Outline each blood parasite and name the species.
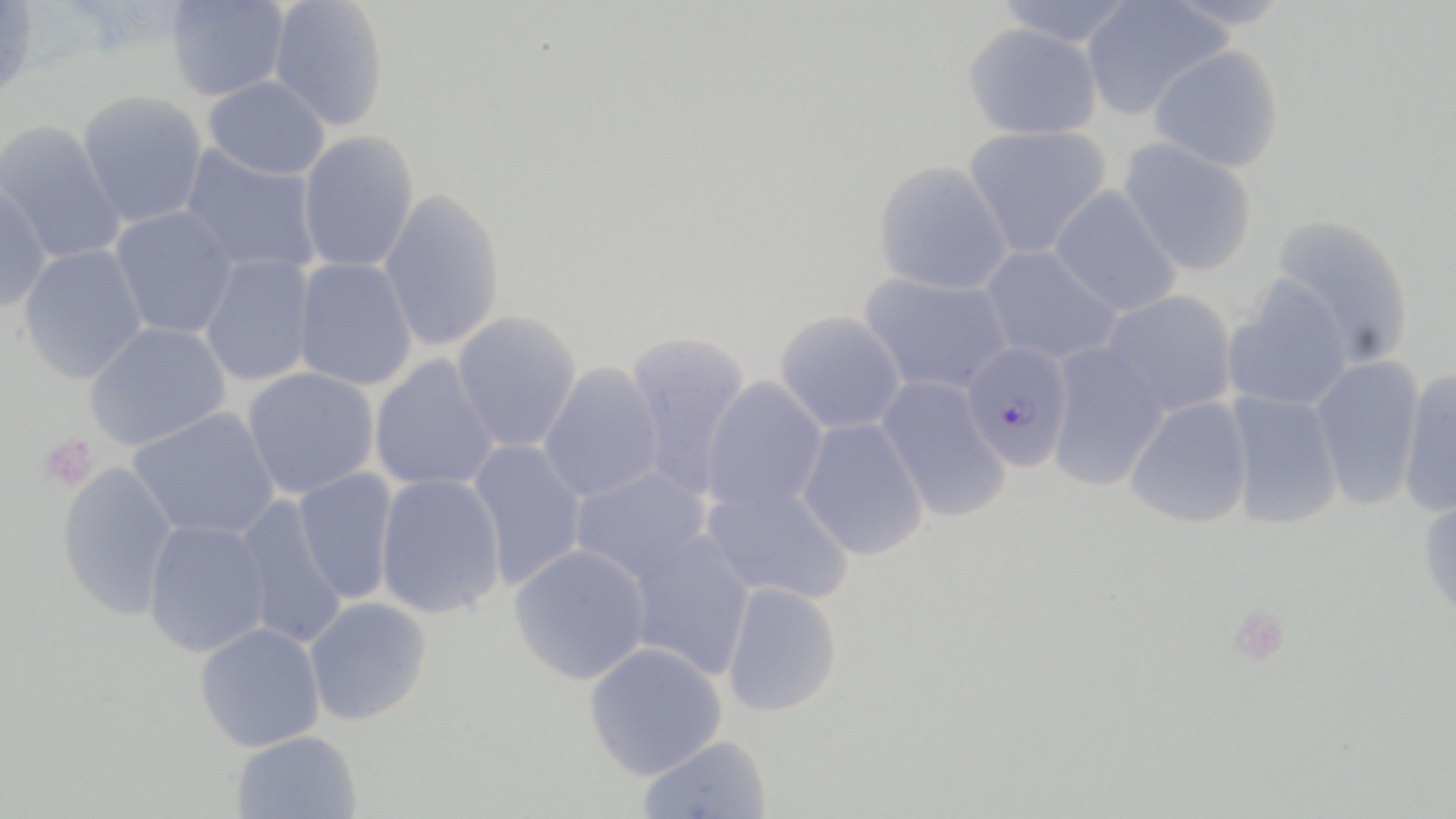
Approximate bounding boxes as (x1,y1)-(x2,y2) corner pairs in pixels.
Plasmodium falciparum-infected red blood cells: (960,341)-(1073,471).
No Plasmodium ovale, Plasmodium malariae, Plasmodium vivax, Babesia divergens, or Trypanosoma brucei observed.

slide-level diagnosis = Plasmodium falciparum
field of view = single
platelet locations = approximate bounding boxes as (x1,y1)-(x2,y2) corner pairs in pixels: (38,434)-(98,490)
preparation = thin blood film
magnification = 1000x
image size = 1456×819 pixels
modality = light microscopy
stain = May-Grünwald-Giemsa
uninfected red blood cell locations = approximate bounding boxes as (x1,y1)-(x2,y2) corner pairs in pixels: (0,0)-(40,101), (993,0)-(1138,48), (1080,0)-(1231,120), (1159,0)-(1294,29), (165,1)-(289,101), (268,1)-(389,132), (963,22)-(1103,140), (1147,44)-(1285,174), (203,76)-(330,180), (77,90)-(208,228), (0,122)-(126,264), (962,125)-(1112,259), (297,131)-(419,272), (1119,137)-(1258,277), (181,145)-(322,275), (873,161)-(1012,296), (0,180)-(51,312), (1049,185)-(1183,317), (378,189)-(505,352), (110,205)-(238,339), (1267,213)-(1416,367), (19,244)-(149,383), (979,245)-(1124,366), (200,254)-(316,387), (293,258)-(417,391), (857,271)-(1013,396), (1222,278)-(1354,412), (1100,290)-(1238,417), (451,311)-(582,452), (774,311)-(907,434), (83,321)-(230,451), (624,330)-(752,497), (1044,341)-(1170,492), (1309,354)-(1426,512), (369,355)-(500,492), (538,362)-(664,503), (1396,366)-(1456,518), (242,367)-(379,499), (700,376)-(829,516), (875,376)-(1012,523), (1222,391)-(1344,530), (1124,397)-(1253,529), (128,407)-(280,540), (796,418)-(929,560), (465,439)-(588,590), (57,461)-(179,620), (569,464)-(711,585), (293,467)-(399,606), (375,473)-(505,619), (702,482)-(854,605), (1417,490)-(1456,629), (232,495)-(347,650), (143,518)-(271,657), (626,530)-(756,680), (509,544)-(651,685), (721,581)-(842,717), (303,596)-(431,725), (194,622)-(325,752), (584,642)-(727,780), (230,730)-(362,818), (636,734)-(773,819)